Classify this cell by malaria status.
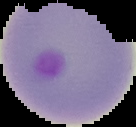
It is parasitized.

image size = 136×127 pixels
preparation = thin blood smear
image type = segmented cell region on a black background